Draw a bounding box around every artifact (stain precipitate or debris).
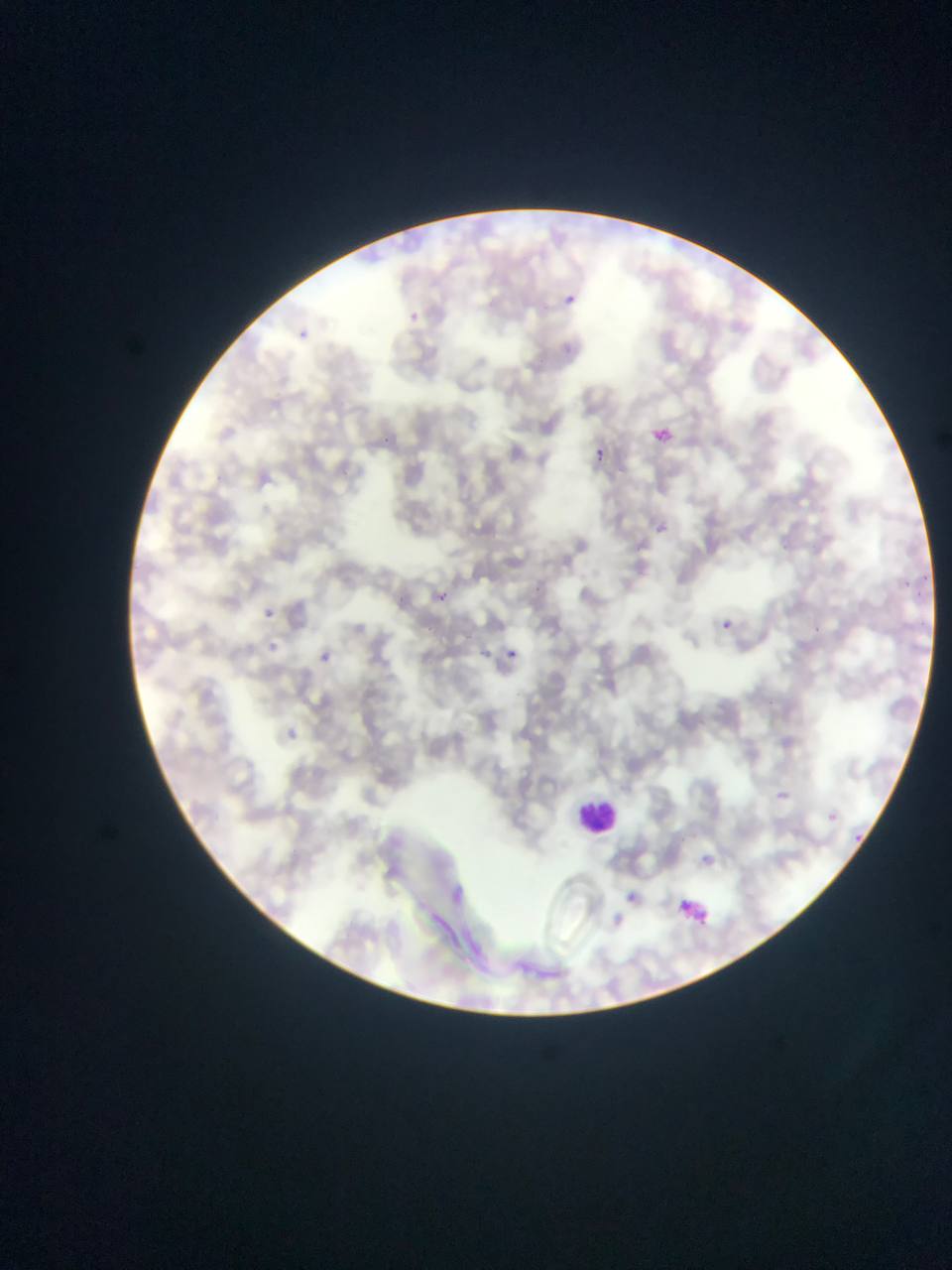

Approximate bounding boxes as {left, top, right, bottom} in pixels.
Artifacts (stain precipitate or debris): {678, 891, 738, 926}.

image_size: 952×1270 pixels
capture: mobile-phone photograph through a microscope
object_labeled_both_plasmodium_parasite_and_leukocyte_by_the_source: 'approximate bounding boxes as {left, top, right, bottom} in pixels: {562, 790, 634, 861}'
plasmodium_parasite_locations: 'approximate bounding boxes as {left, top, right, bottom} in pixels: {557, 283, 600, 326}, {296, 329, 309, 342}, {647, 423, 679, 453}, {591, 446, 612, 468}, {648, 518, 673, 541}, {428, 586, 454, 609}, {252, 601, 281, 630}, {708, 612, 741, 640}, {496, 641, 525, 670}, {313, 648, 336, 669}, {766, 783, 792, 808}, {816, 802, 847, 831}, {690, 846, 721, 873}, {436, 878, 479, 918}, {614, 883, 647, 914}, {599, 902, 636, 938}'
country: Ghana
field_of_view: single
preparation: thin blood smear